Name the cell type shown.
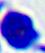

A leukocyte.

magnification = 400x
modality = photomicrograph